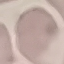
{
  "result": "no malaria parasites detected",
  "image_type": "automatically extracted cell patch, resized to 64 × 64 pixels",
  "capture": "smartphone through the microscope eyepiece",
  "stain": "Giemsa",
  "preparation": "thin smear"
}